State the blood parasite species.
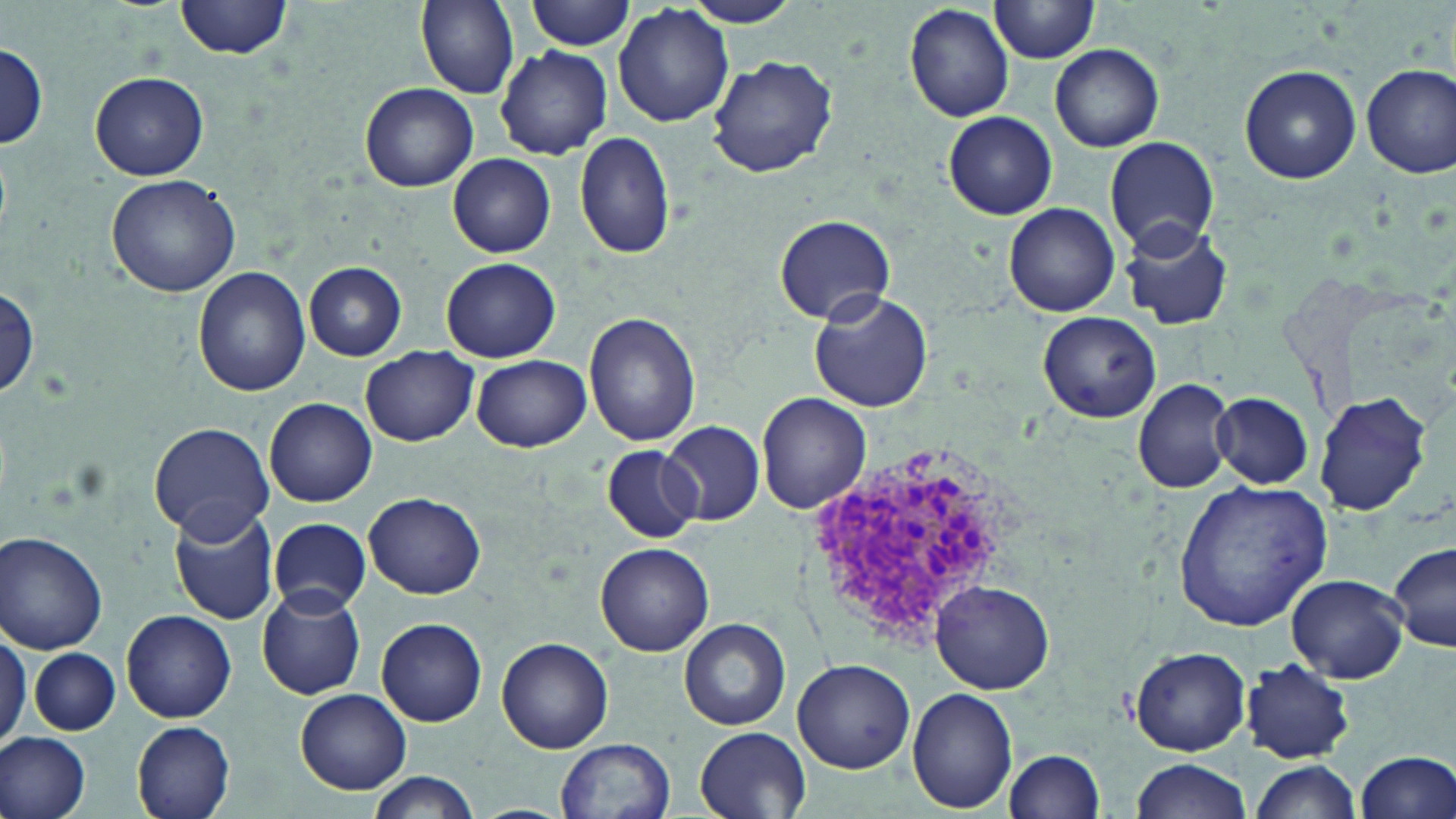

Plasmodium vivax.

Approximate bounding boxes as (x1,y1)-(x2,y2) corner pairs in pixels. Plasmodium vivax-infected red blood cell locations: (800,434)-(1021,653). Uninfected red blood cell locations: (176,0)-(291,59), (414,0)-(521,99), (527,0)-(635,51), (680,0)-(806,27), (989,0)-(1102,63), (903,3)-(1015,123), (613,5)-(735,129), (0,43)-(48,150), (1050,44)-(1164,152), (495,46)-(612,160), (706,57)-(839,177), (1361,63)-(1456,179), (1239,64)-(1362,184), (89,71)-(210,181), (359,83)-(478,192), (941,110)-(1058,220), (574,132)-(676,261), (1103,136)-(1221,257), (448,154)-(556,257), (108,174)-(239,297), (1004,202)-(1120,317), (773,212)-(897,325), (1117,216)-(1233,331), (442,257)-(561,362), (305,261)-(408,360), (193,267)-(311,396), (1,286)-(41,402), (808,290)-(933,413), (584,312)-(702,447), (1036,312)-(1162,423), (362,347)-(478,446), (472,354)-(592,452), (1132,378)-(1235,494), (1211,392)-(1313,488), (1313,392)-(1432,516), (756,394)-(870,514), (265,398)-(377,506), (148,422)-(275,541), (658,422)-(767,527), (602,446)-(702,542), (1173,481)-(1333,630), (365,493)-(485,598), (168,504)-(281,625), (269,518)-(370,615), (0,531)-(108,652), (594,542)-(714,657), (1389,542)-(1455,651), (1283,575)-(1409,682), (932,581)-(1057,692), (257,586)-(366,700), (122,609)-(236,722), (377,617)-(487,727), (679,619)-(791,731), (0,622)-(30,755), (497,636)-(613,753), (30,646)-(120,735), (1130,647)-(1250,755), (792,657)-(915,773), (1242,658)-(1355,762), (907,686)-(1017,812), (296,689)-(411,794), (132,721)-(235,819), (695,726)-(812,817), (1,732)-(92,819), (557,737)-(677,819), (1351,748)-(1456,819), (1002,750)-(1105,819), (1129,759)-(1251,819), (1248,760)-(1361,819), (363,771)-(481,819). Thin blood film. Optical microscopy. Image is 1456×819 pixels. One field of a larger specimen. 1000x magnification. May-Grünwald-Giemsa stain.